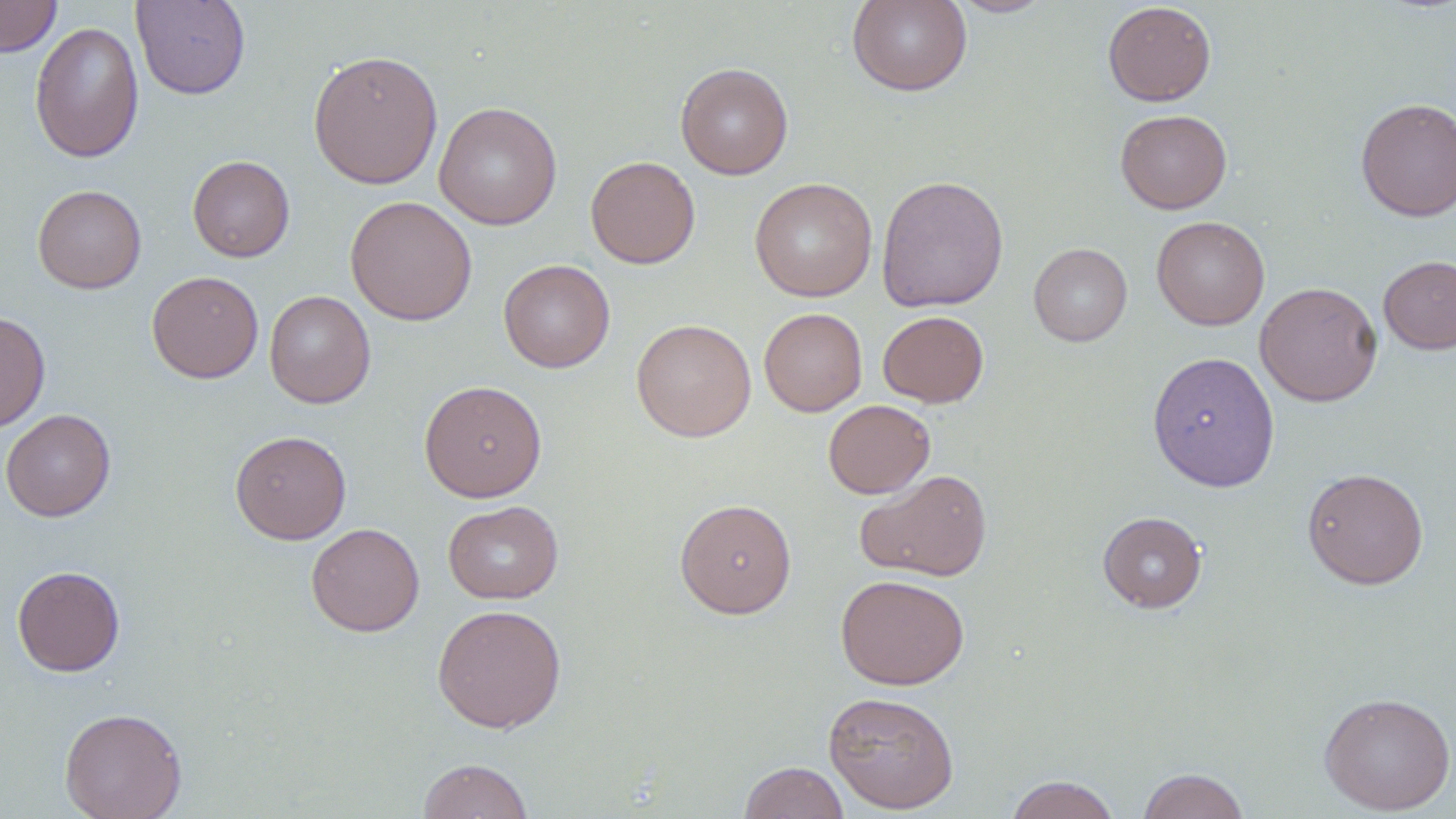
Approximate bounding boxes as (x1,y1)-(x2,y2) corner pairs in pixels. Uninfected red blood cell locations: (0,0)-(61,57), (131,0)-(251,100), (847,0)-(973,96), (949,0)-(1053,17), (1102,1)-(1217,106), (29,22)-(145,164), (307,49)-(443,190), (676,62)-(793,179), (1355,97)-(1456,221), (434,101)-(562,230), (1115,109)-(1232,214), (187,155)-(295,262), (585,155)-(700,269), (875,175)-(1009,312), (749,178)-(877,301), (32,184)-(147,293), (345,196)-(477,325), (1151,215)-(1270,331), (1028,242)-(1132,346), (1378,255)-(1456,354), (499,259)-(615,372), (146,271)-(264,383), (1255,281)-(1382,407), (264,289)-(376,408), (759,308)-(867,416), (0,310)-(51,433), (878,310)-(989,408), (631,319)-(757,441), (1147,351)-(1281,492), (419,380)-(547,502), (823,399)-(935,499), (0,408)-(116,522), (230,430)-(351,544), (1302,467)-(1429,589), (856,469)-(993,582), (675,498)-(797,618), (443,500)-(563,604), (1097,511)-(1207,612), (306,522)-(425,637), (12,565)-(125,676), (835,574)-(970,690), (432,604)-(567,732), (823,690)-(960,814), (1319,692)-(1456,815), (59,707)-(187,819), (417,758)-(535,818), (739,761)-(849,819), (1136,767)-(1251,819), (1004,774)-(1122,819). Slide-level diagnosis: negative for blood parasites. Light microscopy. Image is 1456×819 pixels. 1000x magnification. Thin blood smear. Single field of view. May-Grünwald-Giemsa-stained preparation.